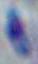
{
  "magnification": "1000x",
  "identification": "Toxoplasma gondii",
  "modality": "micrograph"
}